Give the extent of all uninfected red blood cells.
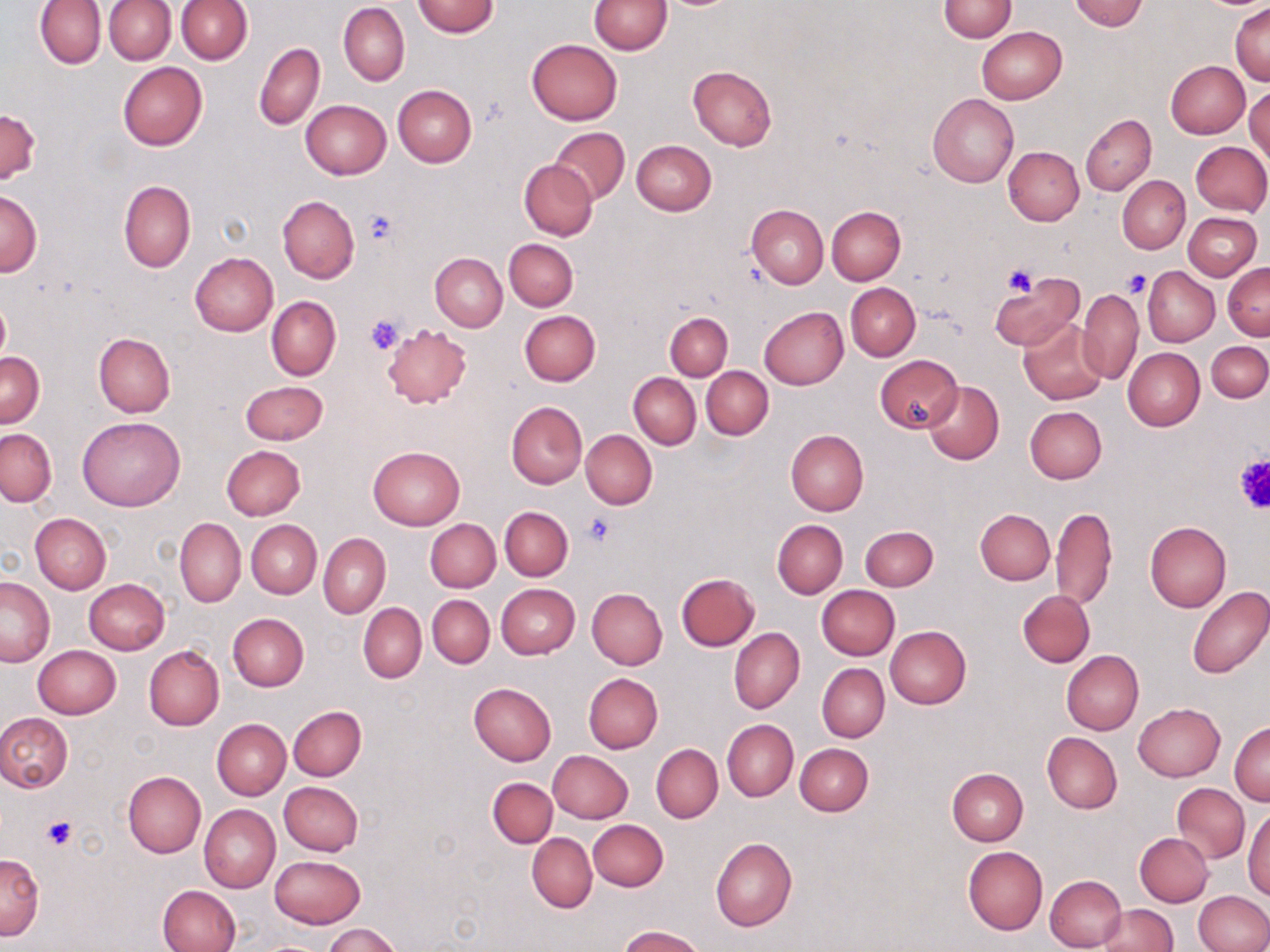

Approximate bounding boxes as (x1, y1, x2, y2) in pixels.
Uninfected red blood cells: (35, 0, 105, 69), (589, 0, 672, 55), (1071, 0, 1147, 31), (105, 1, 175, 64), (176, 1, 253, 64), (412, 1, 499, 37), (939, 1, 1017, 41), (338, 3, 410, 86), (1231, 3, 1270, 85), (977, 26, 1066, 103), (527, 39, 622, 125), (254, 42, 324, 130), (1166, 61, 1250, 138), (118, 62, 207, 150), (688, 65, 777, 150), (392, 84, 476, 166), (1245, 84, 1269, 167), (928, 94, 1018, 188), (301, 100, 390, 179), (0, 107, 40, 183), (1081, 114, 1155, 195), (551, 127, 629, 204), (631, 141, 716, 215), (1190, 141, 1270, 215), (1003, 146, 1084, 226), (519, 160, 597, 240), (1118, 175, 1190, 253), (118, 179, 195, 273), (0, 189, 42, 276), (278, 197, 359, 282), (746, 204, 827, 288), (826, 206, 906, 285), (1183, 212, 1261, 281), (505, 238, 578, 311), (189, 252, 278, 336), (430, 252, 507, 332), (1223, 263, 1270, 339), (1144, 267, 1219, 346), (990, 274, 1084, 354), (846, 283, 920, 361), (1077, 288, 1144, 384), (267, 297, 341, 381), (0, 298, 10, 368), (760, 307, 848, 389), (520, 310, 601, 385), (665, 311, 733, 379), (1018, 317, 1110, 406), (382, 323, 472, 408), (93, 333, 175, 417), (1206, 340, 1270, 402), (1122, 347, 1205, 431), (0, 352, 44, 427), (875, 355, 962, 432), (702, 366, 773, 440), (628, 373, 699, 448), (241, 380, 328, 445), (922, 380, 1003, 464), (506, 402, 587, 488), (1025, 406, 1107, 483), (77, 416, 184, 512), (0, 428, 56, 506), (581, 430, 656, 509), (785, 430, 868, 515), (221, 444, 305, 520), (369, 445, 465, 529), (1051, 506, 1117, 611), (500, 507, 572, 581), (975, 509, 1055, 585), (30, 513, 111, 594), (175, 518, 246, 607), (426, 519, 500, 592), (773, 520, 847, 599), (246, 521, 321, 598), (1144, 522, 1231, 612), (860, 526, 937, 591), (319, 533, 391, 619), (676, 573, 759, 651), (1, 576, 55, 666), (84, 578, 169, 654), (496, 585, 579, 659), (1185, 585, 1269, 679), (817, 586, 900, 660), (586, 588, 667, 669), (1018, 590, 1094, 667), (427, 595, 494, 667), (358, 603, 426, 682), (228, 613, 309, 691), (884, 625, 971, 708), (729, 628, 804, 714), (33, 645, 121, 719), (144, 646, 224, 730), (1061, 650, 1144, 735), (817, 663, 889, 742), (584, 673, 663, 753), (469, 683, 556, 765), (1133, 702, 1225, 781), (289, 705, 367, 781), (0, 712, 74, 794), (211, 719, 290, 800), (722, 720, 797, 801), (1230, 722, 1269, 805), (1042, 733, 1122, 813), (651, 744, 723, 823), (795, 744, 873, 816), (548, 750, 634, 823), (948, 767, 1028, 845), (123, 771, 206, 857), (488, 778, 558, 848), (280, 781, 364, 856), (1173, 784, 1249, 862), (1244, 803, 1270, 899), (200, 805, 280, 893), (588, 820, 669, 891), (527, 832, 597, 913), (1135, 832, 1213, 906), (710, 838, 797, 931), (962, 846, 1047, 934), (0, 852, 44, 940), (271, 855, 364, 928), (1043, 874, 1127, 951), (156, 885, 240, 952), (1194, 891, 1270, 951), (1097, 903, 1178, 952), (324, 923, 402, 952), (618, 926, 705, 952).

slide-level diagnosis = no evidence of blood parasites
field of view = one of a larger specimen
modality = light microscopy
image size = 1270×952 pixels
stain = May-Grünwald-Giemsa
platelet locations = approximate bounding boxes as (x1, y1, x2, y2) in pixels: (364, 208, 401, 246), (1002, 265, 1037, 297), (1124, 268, 1152, 298), (365, 315, 404, 356), (1232, 453, 1270, 514), (586, 514, 615, 546), (40, 815, 78, 850)
magnification = 1000x
preparation = thin blood film